Assess for Plasmodium parasites.
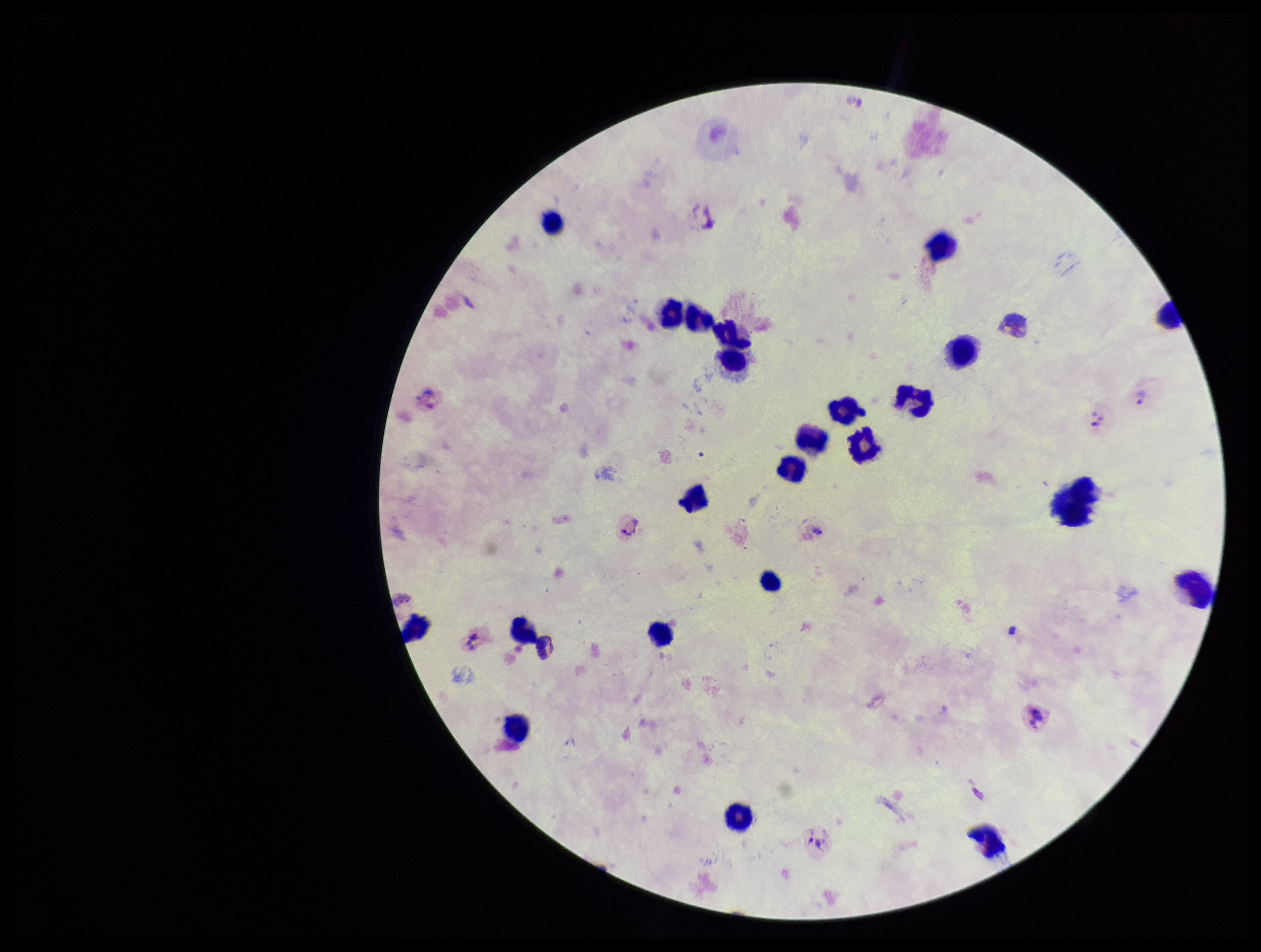
Seen.

Summary:
  - Image size: 1261×952 pixels
  - Leukocyte count: 23
  - Parasite count: 3
  - Capture: smartphone photograph through the microscope eyepiece
  - Field of view: one from this slide
  - Preparation: thick smear
  - Patient malaria status: positive
  - Stain: Giemsa
  - Species reported for this patient: Plasmodium vivax